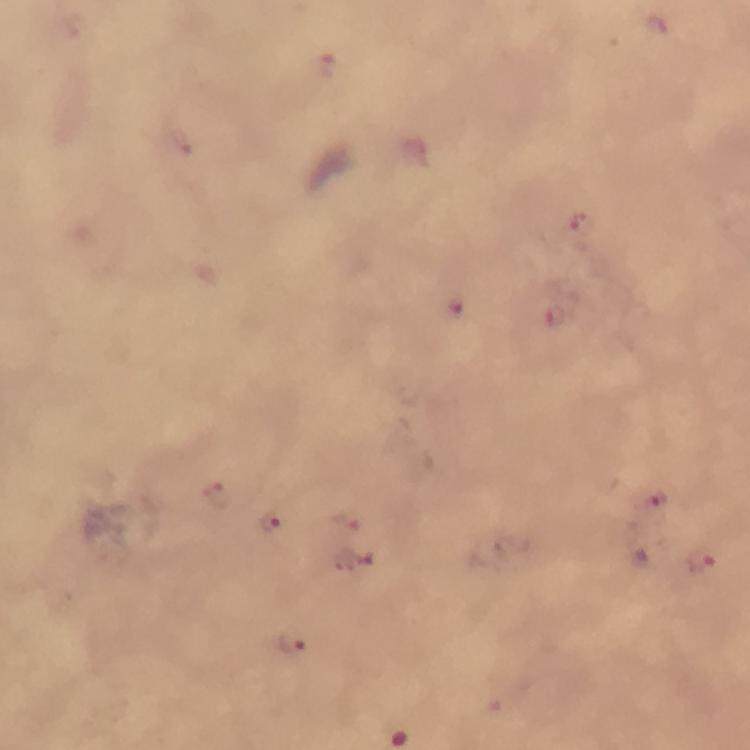

cropped from = one field of view
immersion oil = used
stain = Giemsa
preparation = thick blood film
Plasmodium parasite locations = approximate object centers, in pixels from the top-left corner: (x=326, y=63), (x=577, y=222), (x=455, y=309), (x=555, y=315), (x=219, y=494), (x=652, y=499), (x=270, y=519), (x=345, y=521), (x=356, y=557), (x=701, y=561), (x=293, y=647)
capture = smartphone mounted on the microscope
context = from a malaria diagnostic workup
magnification = 100x
image size = 750×750 pixels